Assess this cell for malaria.
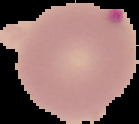

It is parasitized.

The area outside the segmented cell region is set to black. Image is 139×124 pixels. From a thin blood film.